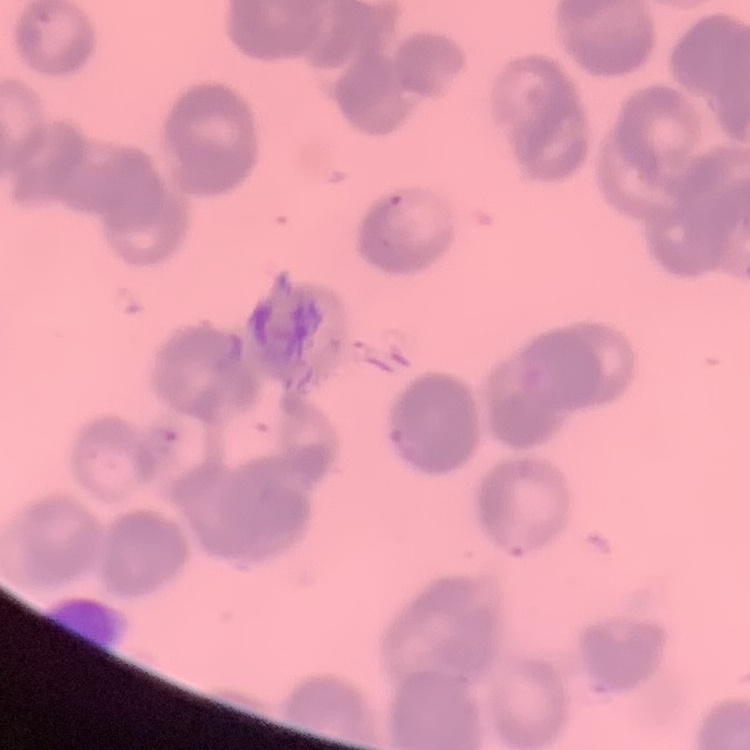 The erythrocytes exhibit rouleaux formation. Square crop of a larger photomicrograph. Thin peripheral smear. Field's or Giemsa stain.